Mark where platelets are.
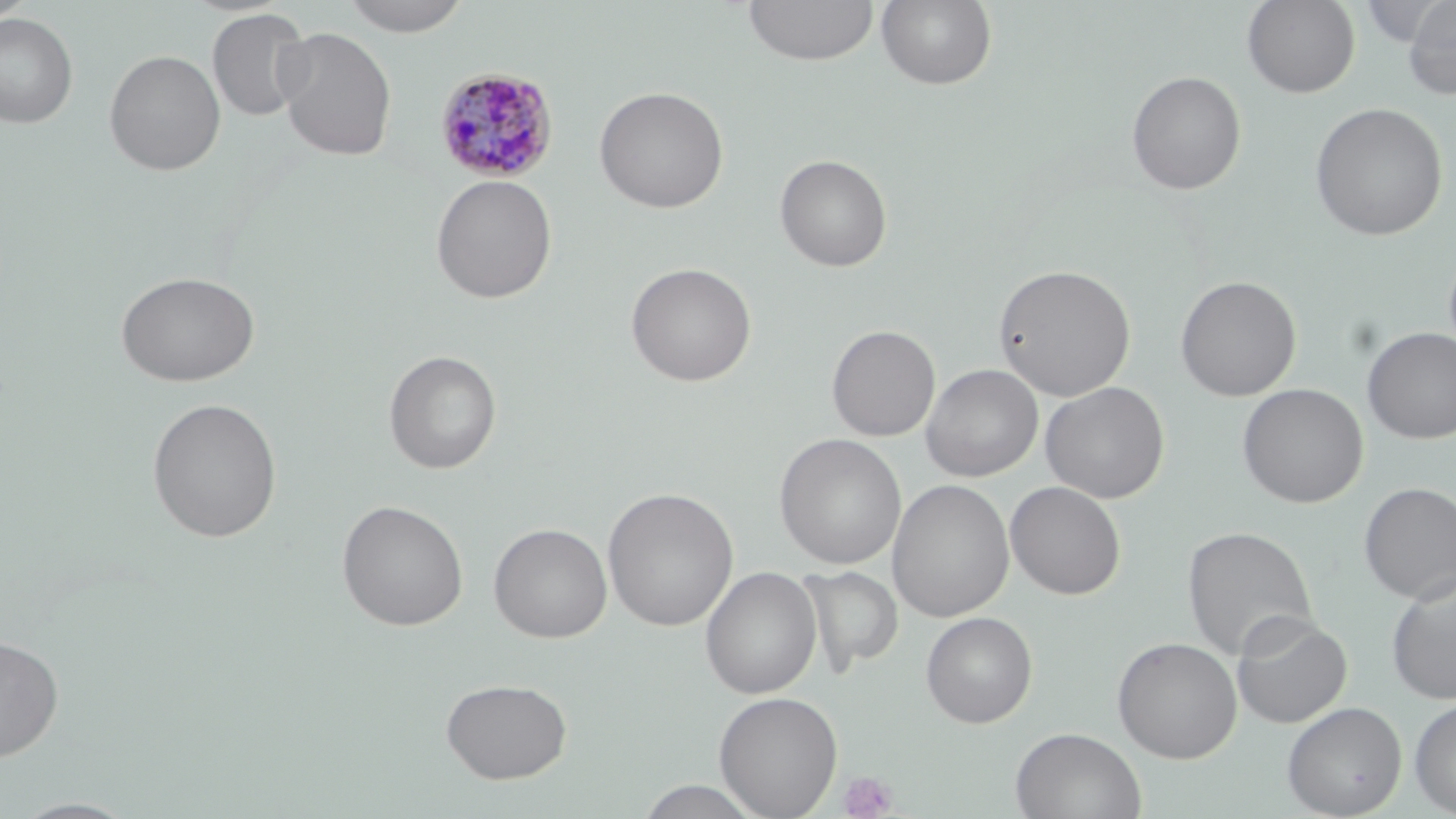
Approximate bounding boxes as (x1,y1)-(x2,y2) corner pairs in pixels.
Platelets: (839,771)-(897,818).

slide-level diagnosis = Plasmodium malariae
uninfected red blood cell locations = approximate bounding boxes as (x1,y1)-(x2,y2) corner pairs in pixels: (1,0)-(36,24), (338,0)-(475,36), (743,0)-(880,66), (876,0)-(998,90), (1242,0)-(1360,97), (1402,0)-(1456,100), (206,7)-(312,122), (0,12)-(78,128), (273,26)-(398,161), (103,49)-(226,176), (1126,70)-(1247,195), (593,85)-(729,214), (1310,102)-(1448,241), (774,154)-(892,272), (430,174)-(557,304), (625,262)-(757,387), (993,264)-(1136,401), (115,271)-(260,387), (1175,275)-(1302,401), (826,324)-(941,442), (1362,327)-(1456,444), (383,350)-(502,474), (921,363)-(1043,482), (1039,381)-(1170,504), (1237,383)-(1369,508), (146,397)-(283,543), (774,433)-(906,569), (886,479)-(1015,623), (1005,481)-(1127,600), (1358,481)-(1456,604), (602,487)-(739,631), (336,499)-(469,631), (488,522)-(613,643), (1182,525)-(1318,662), (797,565)-(904,674), (700,566)-(822,699), (1385,570)-(1456,705), (1230,611)-(1352,728), (920,612)-(1038,728), (0,633)-(64,762), (1112,637)-(1242,764), (440,677)-(572,784), (713,691)-(843,818), (1409,696)-(1456,817), (1281,701)-(1407,818), (1011,727)-(1147,819), (635,780)-(766,818), (9,797)-(141,818)
preparation = thin blood smear
magnification = 1000x
field of view = one of a larger specimen
Plasmodium malariae-infected red blood cell locations = approximate bounding boxes as (x1,y1)-(x2,y2) corner pairs in pixels: (434,66)-(559,184)
image size = 1456×819 pixels
stain = May-Grünwald-Giemsa
modality = optical microscopy